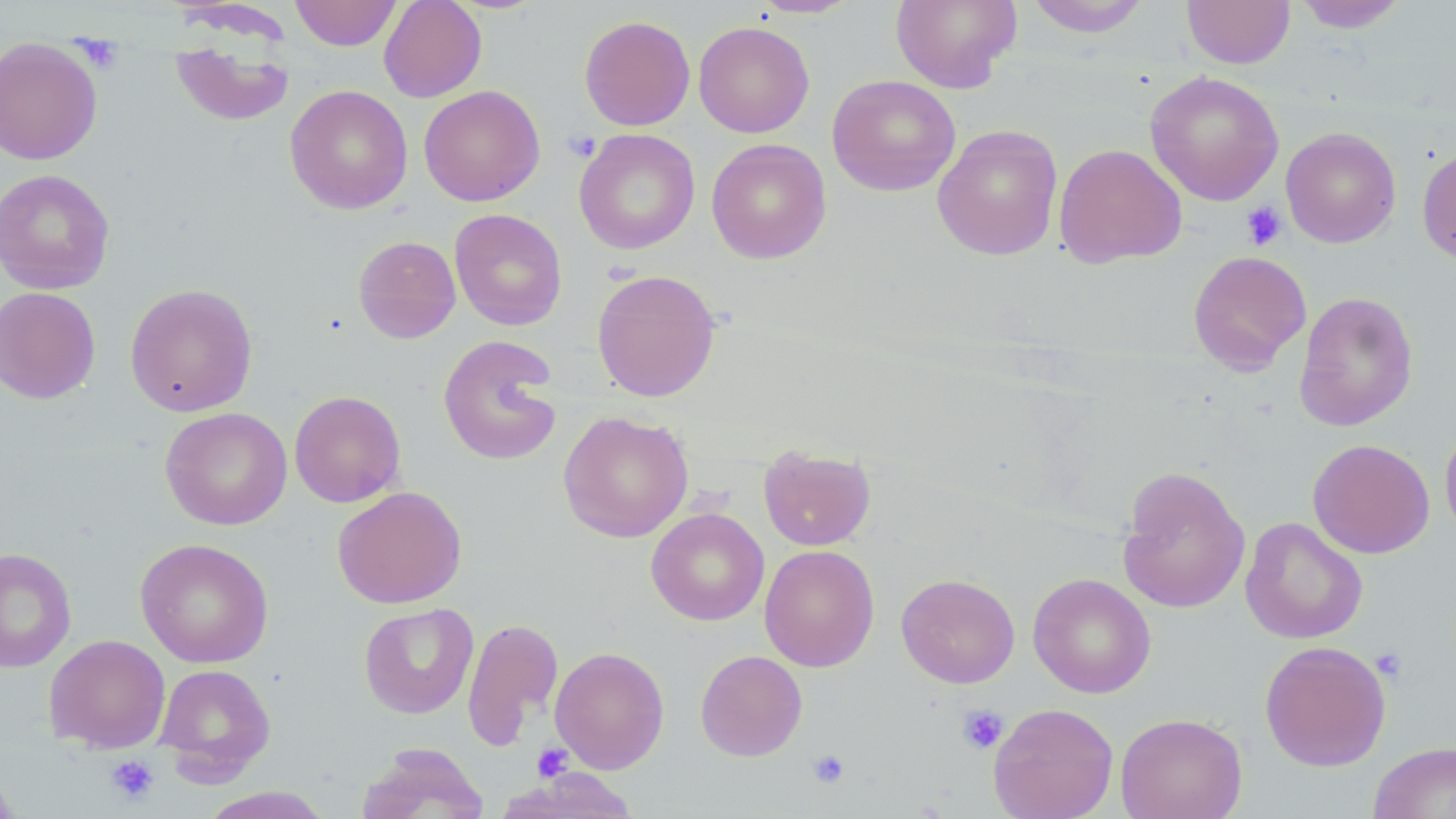
Approximate bounding boxes as (x1,y1)-(x2,y2) corner pairs in pixels. Uninfected red blood cell locations: (290,0)-(401,50), (379,0)-(487,103), (749,0)-(862,19), (890,0)-(1022,93), (1025,0)-(1150,38), (1182,0)-(1295,68), (1293,1)-(1408,33), (579,15)-(696,131), (693,21)-(814,138), (0,37)-(103,165), (170,37)-(294,126), (1145,70)-(1285,207), (827,74)-(961,196), (285,85)-(413,214), (418,85)-(545,206), (932,124)-(1063,261), (1281,127)-(1401,248), (574,129)-(700,254), (706,138)-(832,264), (1053,143)-(1187,268), (1417,145)-(1456,267), (0,168)-(115,294), (449,208)-(567,331), (353,235)-(461,344), (1187,250)-(1312,375), (592,268)-(721,402), (125,283)-(257,417), (0,286)-(101,405), (1294,290)-(1419,431), (438,335)-(562,466), (289,390)-(406,507), (160,407)-(292,530), (558,410)-(694,543), (1440,423)-(1456,543), (1308,439)-(1435,559), (758,445)-(876,551), (1117,465)-(1251,614), (332,486)-(467,609), (646,507)-(769,625), (1240,517)-(1368,644), (135,538)-(273,668), (759,545)-(880,672), (0,547)-(76,673), (896,572)-(1020,688), (1028,572)-(1156,698), (358,602)-(478,719), (461,617)-(563,751), (44,634)-(170,753), (1259,640)-(1391,771), (550,646)-(669,774), (695,649)-(808,761), (154,663)-(275,782), (989,702)-(1119,819), (1115,712)-(1248,819), (1368,741)-(1456,819), (358,742)-(490,819), (0,762)-(19,819), (506,768)-(638,818), (195,787)-(335,818). Platelet locations: (73,35)-(124,73), (563,130)-(602,162), (1241,201)-(1288,251), (1371,646)-(1409,683), (957,704)-(1009,755), (533,743)-(573,781), (806,749)-(851,789), (105,755)-(159,806). Slide-level diagnosis: no evidence of blood parasites. Image is 1456×819 pixels. 1000x magnification. May-Grünwald-Giemsa stain. Light microscopy. Thin blood film. One field of a larger specimen.